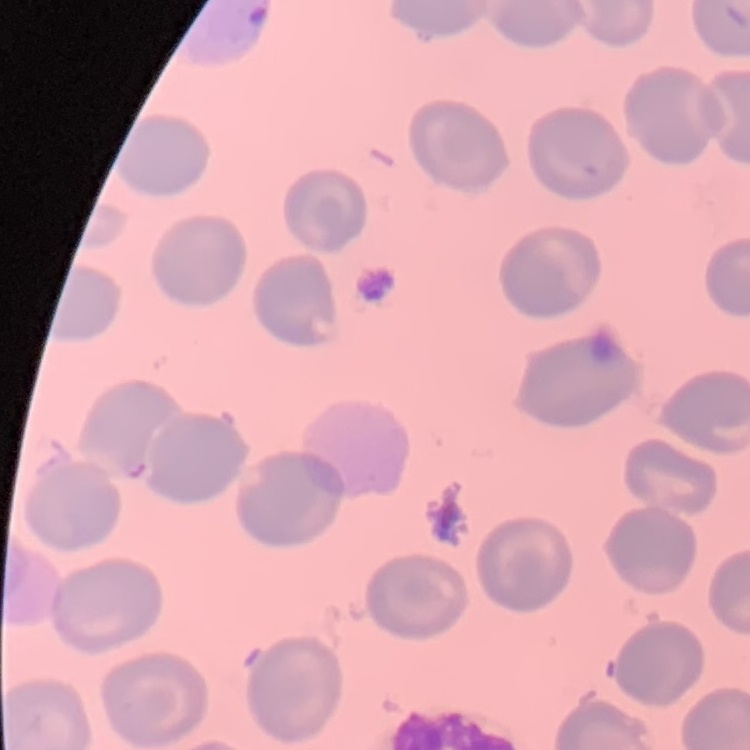
The red blood cells exhibit no rouleaux formation. Stained with either Field's or Giemsa. Thin peripheral smear. One tile cut from a larger photomicrograph.